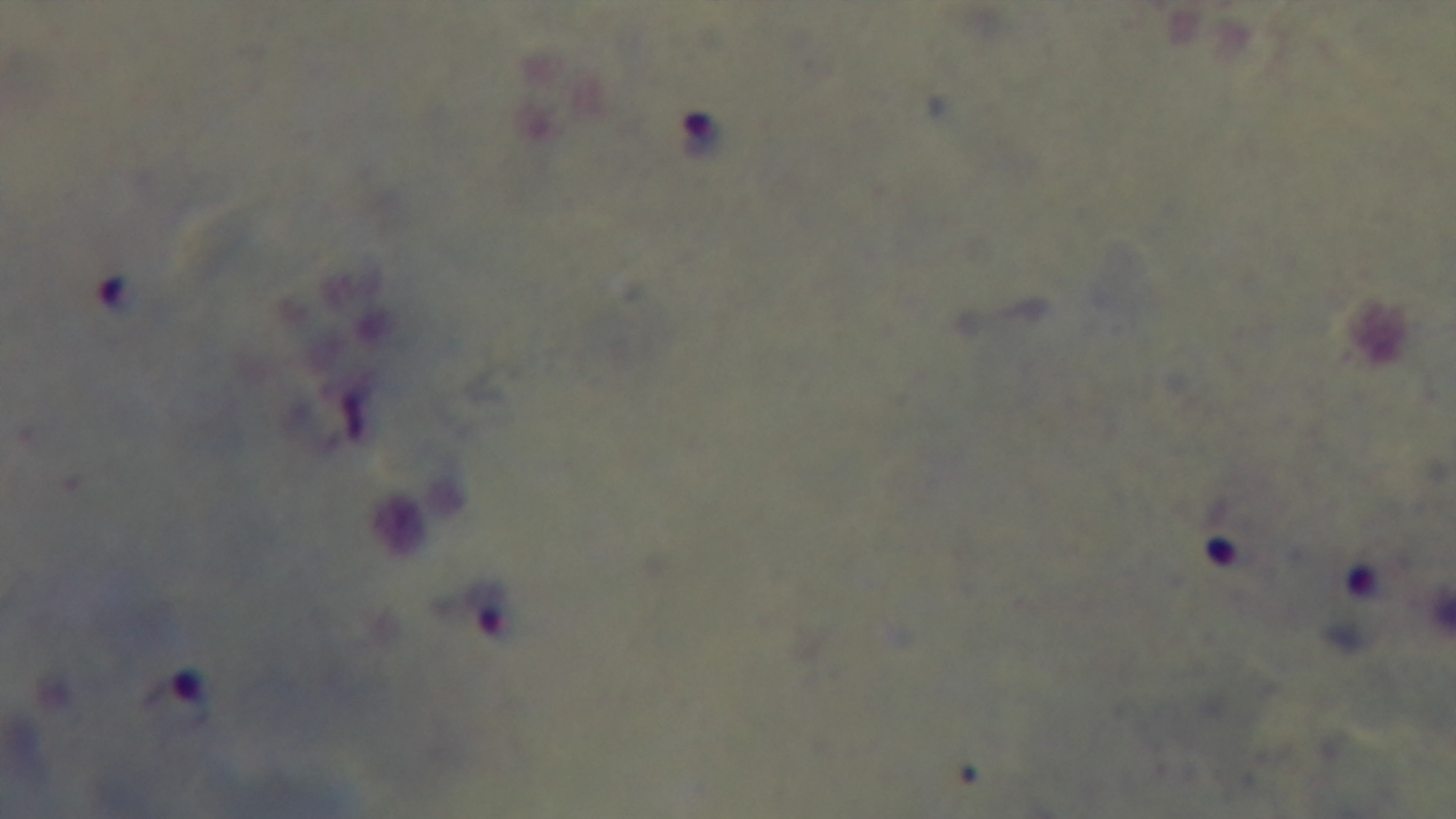

capture: mounted 4K digital camera
objective: 100x oil immersion
modality: light microscopy
field_of_view: single
malaria_status: positive
preparation: thick smear
stain: Giemsa